State which cell type is depicted.
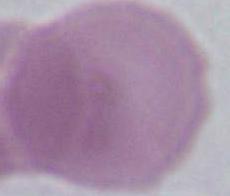
An erythrocyte.

modality = micrograph
magnification = 1000x